Locate every blood parasite and identify its species.
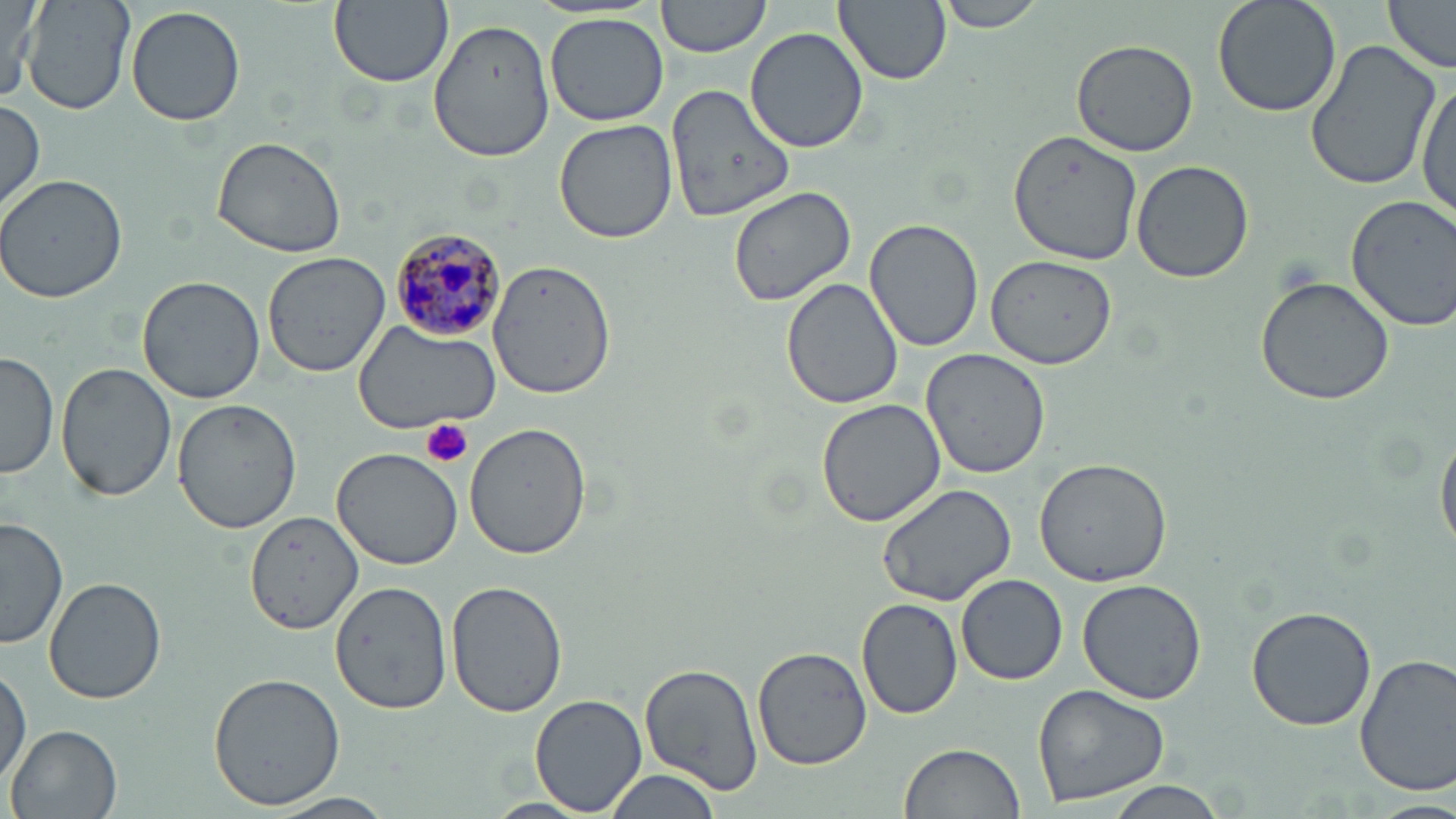

Approximate bounding boxes as (x1,y1)-(x2,y2) corner pairs in pixels.
Plasmodium malariae-infected red blood cells: (389,226)-(509,341).
No Plasmodium falciparum, Plasmodium ovale, Plasmodium vivax, Babesia divergens, or Trypanosoma brucei observed.

Platelet locations: (422,418)-(474,469). Uninfected red blood cell locations: (2,0)-(46,107), (22,0)-(133,117), (329,0)-(453,88), (656,0)-(770,58), (835,0)-(950,87), (934,0)-(1049,33), (1210,0)-(1341,120), (1384,0)-(1456,73), (126,6)-(246,128), (546,14)-(667,126), (429,17)-(552,160), (744,28)-(870,153), (1071,36)-(1202,156), (1303,36)-(1444,192), (1416,80)-(1455,229), (666,85)-(795,222), (0,101)-(48,219), (552,118)-(678,244), (1008,132)-(1144,265), (211,135)-(351,258), (1131,159)-(1253,284), (1,172)-(129,303), (726,186)-(859,309), (1343,193)-(1456,332), (865,218)-(985,352), (261,250)-(390,377), (983,254)-(1117,368), (489,259)-(617,399), (138,275)-(264,404), (1253,276)-(1394,406), (781,279)-(904,410), (351,322)-(501,432), (0,350)-(59,480), (920,350)-(1051,479), (58,362)-(177,503), (815,396)-(949,527), (173,397)-(302,535), (465,423)-(592,560), (1436,425)-(1456,559), (331,446)-(466,570), (1034,458)-(1174,586), (876,481)-(1019,608), (238,508)-(369,633), (0,517)-(67,651), (956,574)-(1067,684), (44,576)-(166,704), (1076,577)-(1207,704), (446,580)-(567,720), (332,582)-(450,712), (857,597)-(965,720), (1246,606)-(1378,732), (752,646)-(874,771), (1355,652)-(1456,798), (640,663)-(763,795), (1,664)-(30,792), (208,672)-(347,809), (1031,682)-(1171,807), (530,694)-(647,816), (8,723)-(124,819), (898,743)-(1025,819), (604,772)-(725,819), (1101,778)-(1230,819), (273,792)-(396,818), (1365,797)-(1455,819), (482,798)-(595,818). Slide-level diagnosis: Plasmodium malariae. Light microscopy. Image is 1456×819 pixels. Thin blood film. One field of a larger specimen. Captured at 1000x magnification. May-Grünwald-Giemsa stain.